State which cell type is depicted.
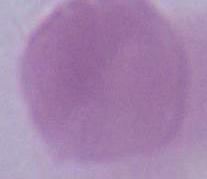
An erythrocyte.

1000x magnification. Photomicrograph.